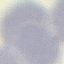

malaria status = uninfected
image type = automatically extracted cell patch, resized to 64 × 64 pixels
stain = Giemsa
preparation = thin blood smear
capture = smartphone camera at the microscope eyepiece